Report the malaria status of this cell.
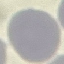
Uninfected.

Photographed with a smartphone camera at the microscope eyepiece. Thin blood film. Giemsa stain. Automatically extracted cell patch, resized to 64 × 64 pixels.